Evaluate for Plasmodium parasites.
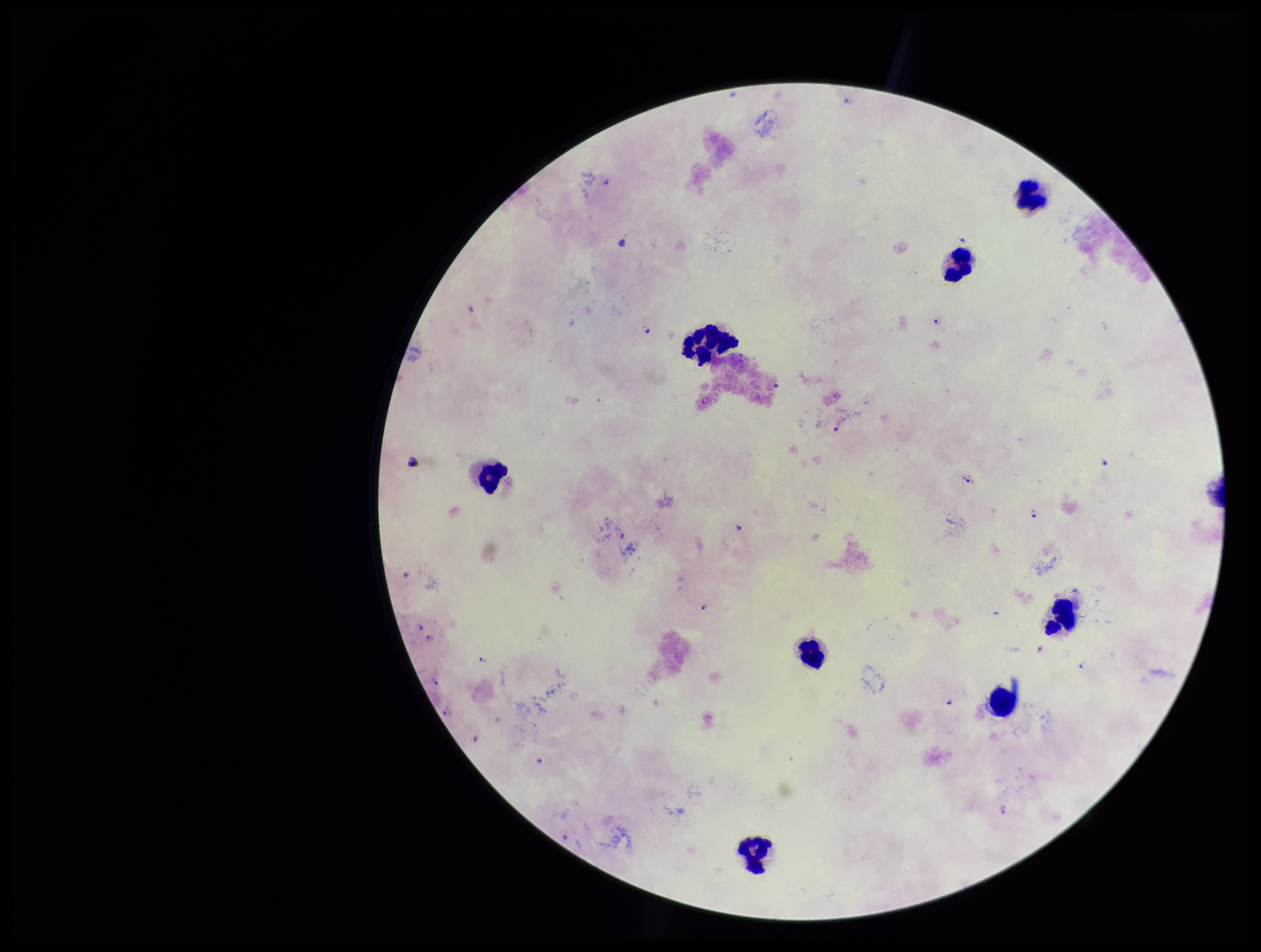

Seen.

capture = smartphone photograph through the microscope eyepiece
leukocyte count = 8
patient malaria status = infected
image size = 1261×952 pixels
stain = Giemsa
field of view = single
species reported for this patient = Plasmodium falciparum
parasite count = 13
preparation = thick blood smear